Comment on the morphology of the red blood cells.
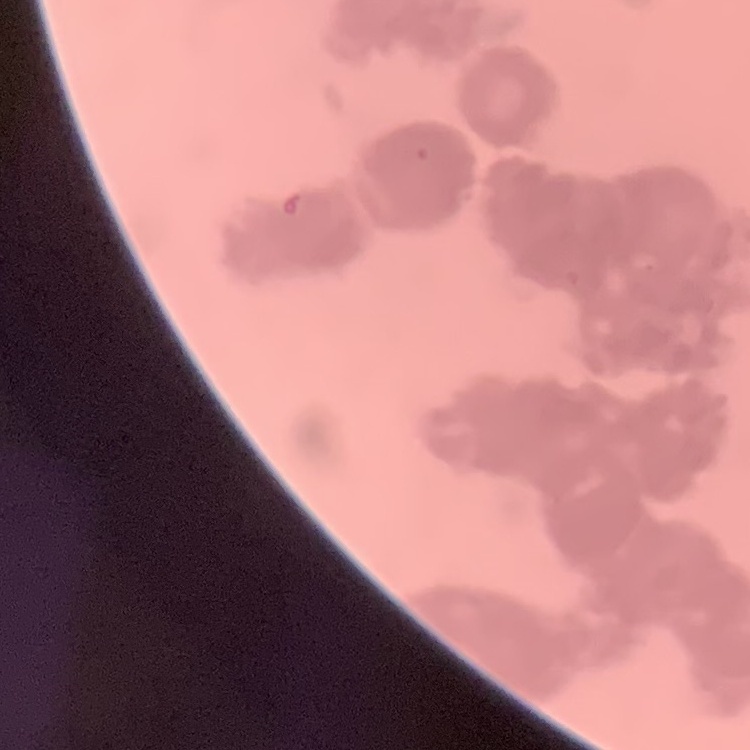

Rouleaux formation.

image type = square crop of a larger photomicrograph
preparation = thin blood film
stain = Field's or Giemsa